Identify the parasite.
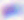

Toxoplasma gondii.

magnification: 400x
modality: photomicrograph